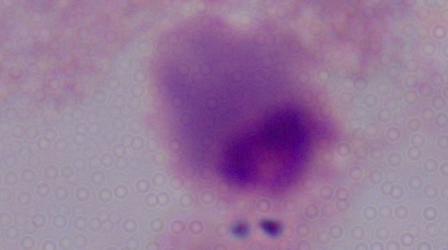

modality = micrograph
identification = trichomonad
magnification = 1000x